State which parasite is depicted.
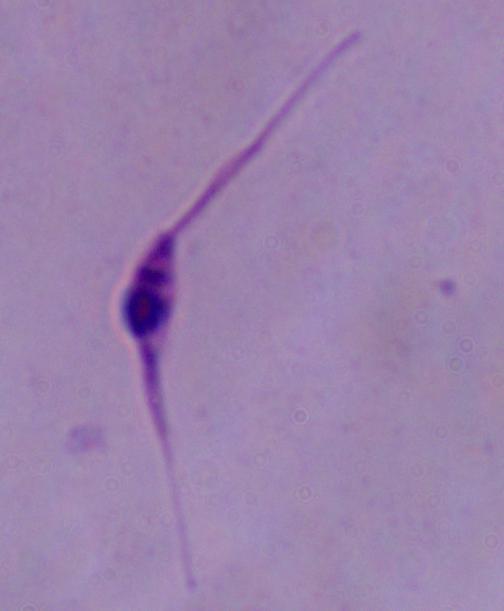

This is Leishmania.

Summary:
  - Modality: photomicrograph
  - Magnification: 1000x